State which parasite is depicted.
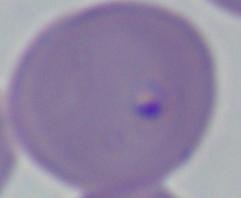

Babesia.

Summary:
  - Magnification: 1000x
  - Modality: micrograph